Locate every blood parasite and identify its species.
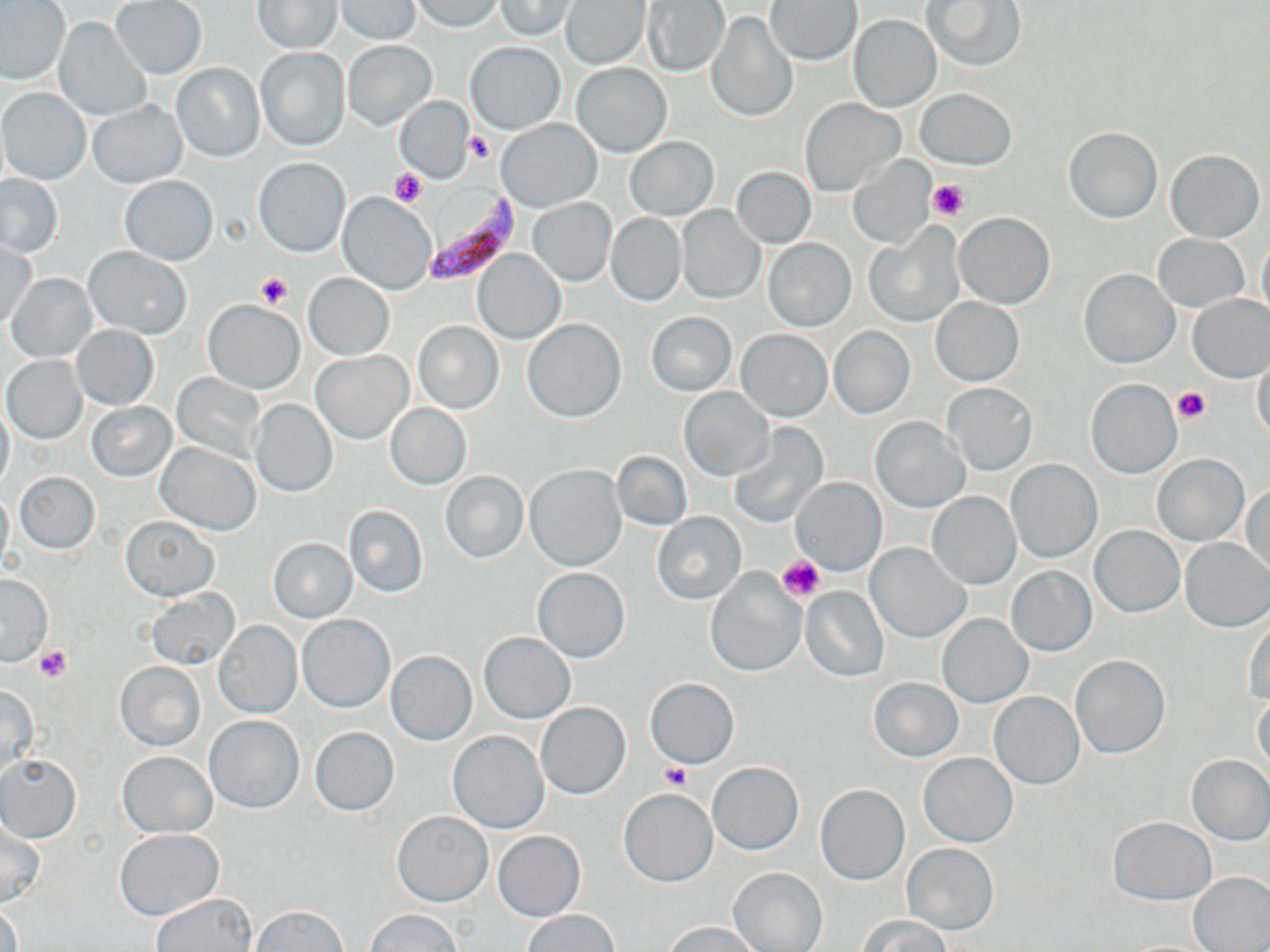
Approximate bounding boxes as (x1,y1)-(x2,y2) corner pairs in pixels.
Plasmodium falciparum-infected red blood cells: (419,193)-(519,287).
No Plasmodium ovale, Plasmodium malariae, Plasmodium vivax, Babesia divergens, or Trypanosoma brucei observed.

Summary:
  - Uninfected red blood cell locations: (335,0)-(421,44), (409,0)-(503,33), (495,0)-(574,40), (922,0)-(1026,72), (109,1)-(207,80), (253,1)-(341,54), (560,1)-(650,69), (642,1)-(729,75), (766,1)-(861,64), (0,2)-(69,86), (706,14)-(796,124), (848,14)-(941,113), (55,18)-(150,121), (343,40)-(436,129), (467,42)-(564,133), (256,47)-(350,151), (171,63)-(265,162), (572,64)-(672,157), (0,88)-(91,185), (917,89)-(1017,169), (395,97)-(473,184), (87,99)-(187,188), (799,100)-(905,197), (496,117)-(601,211), (1063,127)-(1162,223), (625,136)-(718,221), (1165,148)-(1265,243), (846,156)-(937,249), (254,158)-(350,257), (732,166)-(816,248), (0,175)-(63,258), (119,176)-(218,265), (338,192)-(436,294), (528,198)-(615,286), (676,205)-(764,304), (606,213)-(685,306), (954,213)-(1054,309), (865,227)-(964,326), (1153,234)-(1249,313), (1255,235)-(1270,331), (764,240)-(855,331), (1,243)-(38,331), (83,247)-(192,340), (472,249)-(564,344), (1079,270)-(1179,368), (7,273)-(95,362), (303,273)-(395,358), (1186,294)-(1270,382), (931,298)-(1024,386), (202,300)-(305,393), (646,312)-(736,396), (523,319)-(625,422), (414,322)-(503,413), (71,325)-(158,410), (829,326)-(916,419), (736,330)-(831,422), (312,351)-(412,444), (1249,354)-(1269,442), (3,356)-(86,443), (171,373)-(266,464), (1085,379)-(1181,479), (940,383)-(1038,476), (679,388)-(774,480), (250,400)-(336,497), (0,401)-(15,491), (88,402)-(175,482), (386,404)-(471,488), (869,417)-(970,513), (730,424)-(828,529), (157,442)-(261,535), (612,451)-(691,532), (1153,455)-(1248,545), (1007,460)-(1101,563), (525,464)-(625,571), (439,470)-(528,565), (16,471)-(99,553), (791,477)-(886,575), (1243,484)-(1270,579), (927,492)-(1020,590), (343,504)-(428,599), (652,512)-(746,605), (120,513)-(219,601), (1089,525)-(1185,618), (268,538)-(356,624), (1181,539)-(1270,632), (866,543)-(970,642), (1006,566)-(1097,657), (531,567)-(630,662), (704,571)-(804,678), (1,573)-(53,667), (800,587)-(888,681), (145,589)-(241,671), (937,613)-(1033,709), (296,615)-(395,712), (213,620)-(302,719), (1244,621)-(1270,706), (479,632)-(575,723), (386,650)-(477,745), (1072,656)-(1167,759), (115,660)-(205,752), (869,677)-(963,762), (645,678)-(739,769), (0,684)-(39,783), (990,692)-(1083,790), (1250,692)-(1269,774), (536,702)-(630,799), (204,715)-(304,814), (309,726)-(399,817), (447,731)-(549,833), (117,752)-(217,837), (918,752)-(1018,847), (0,753)-(82,844), (1186,754)-(1270,846), (707,762)-(804,854), (814,784)-(909,886), (618,788)-(717,887), (392,811)-(492,906), (1108,817)-(1216,906), (0,822)-(45,908), (114,830)-(224,921), (494,831)-(585,921), (901,843)-(999,935), (727,867)-(828,952), (1189,872)-(1270,952), (151,894)-(259,952), (0,902)-(23,952), (251,904)-(350,951), (365,908)-(465,951), (522,908)-(619,951), (855,914)-(954,952), (665,921)-(760,952)
  - Platelet locations: (465,131)-(495,163), (391,168)-(426,206), (927,177)-(971,221), (256,271)-(293,309), (1173,386)-(1211,424), (777,556)-(825,602), (35,646)-(71,683), (663,763)-(692,790)
  - Slide-level diagnosis: Plasmodium falciparum
  - Stain: May-Grünwald-Giemsa
  - Preparation: thin blood smear
  - Magnification: 1000x
  - Image size: 1270×952 pixels
  - Field of view: single
  - Modality: light microscopy